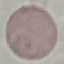
result = negative for malaria parasites
image type = automatically extracted cell patch, resized to 64 × 64 pixels
preparation = thin blood film
stain = Giemsa
capture = smartphone through the microscope eyepiece